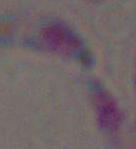
Summary:
  - Magnification: 1000x
  - Identification: Toxoplasma gondii
  - Modality: photomicrograph